Comment on the morphology of the erythrocytes.
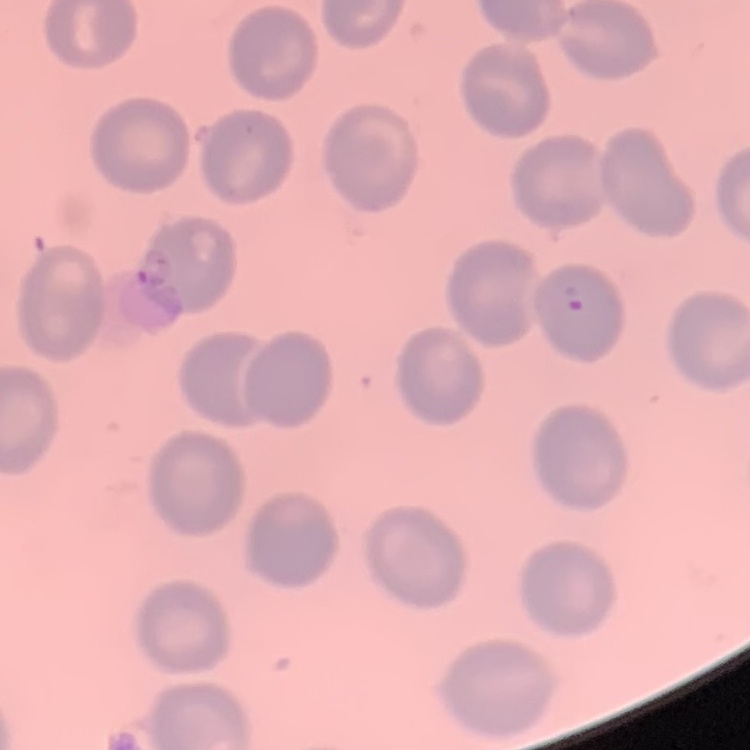

No rouleaux formation.

One tile cut from a larger photomicrograph. Stained with either Field's or Giemsa. Thin blood film.